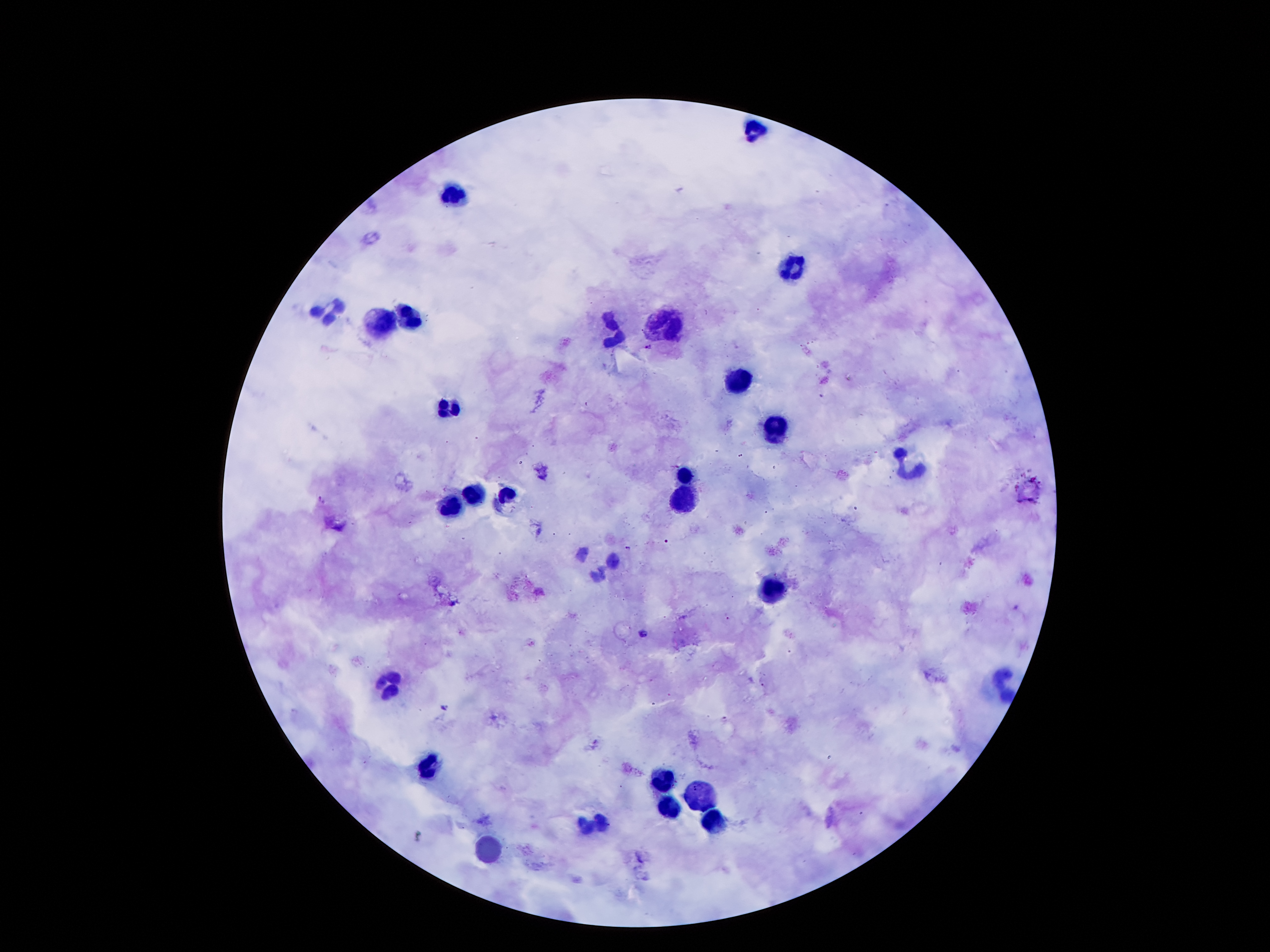
Approximate object centers, in pixels from the top-left corner.
Summary:
  - Leukocyte locations: (x=757, y=130), (x=454, y=195), (x=793, y=267), (x=332, y=312), (x=413, y=320), (x=665, y=325), (x=379, y=326), (x=619, y=331), (x=738, y=381), (x=451, y=405), (x=773, y=432), (x=912, y=465), (x=683, y=473), (x=688, y=491), (x=476, y=493), (x=508, y=496), (x=450, y=505), (x=769, y=594), (x=392, y=684), (x=433, y=768), (x=659, y=780), (x=703, y=796), (x=670, y=812), (x=715, y=821), (x=590, y=823), (x=488, y=850)
  - Malaria parasite locations: (x=649, y=347), (x=320, y=501), (x=628, y=547), (x=643, y=633), (x=763, y=686), (x=445, y=707), (x=724, y=718)
  - Patient malaria status: infected with Plasmodium falciparum
  - Stain: Giemsa
  - Capture: smartphone camera through the microscope eyepiece
  - Field of view: one from this slide
  - Image size: 1270×952 pixels
  - Magnification: 100x
  - Preparation: thick peripheral-blood smear